Assess this cell for malaria.
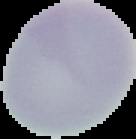

Uninfected.

image size = 136×139 pixels
preparation = thin blood film
image type = segmented cell region with the area outside set to black